State which cell type is depicted.
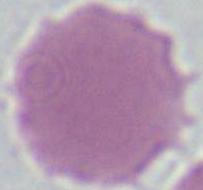

An erythrocyte.

Summary:
  - Magnification: 1000x
  - Modality: photomicrograph